Identify the preparation type.
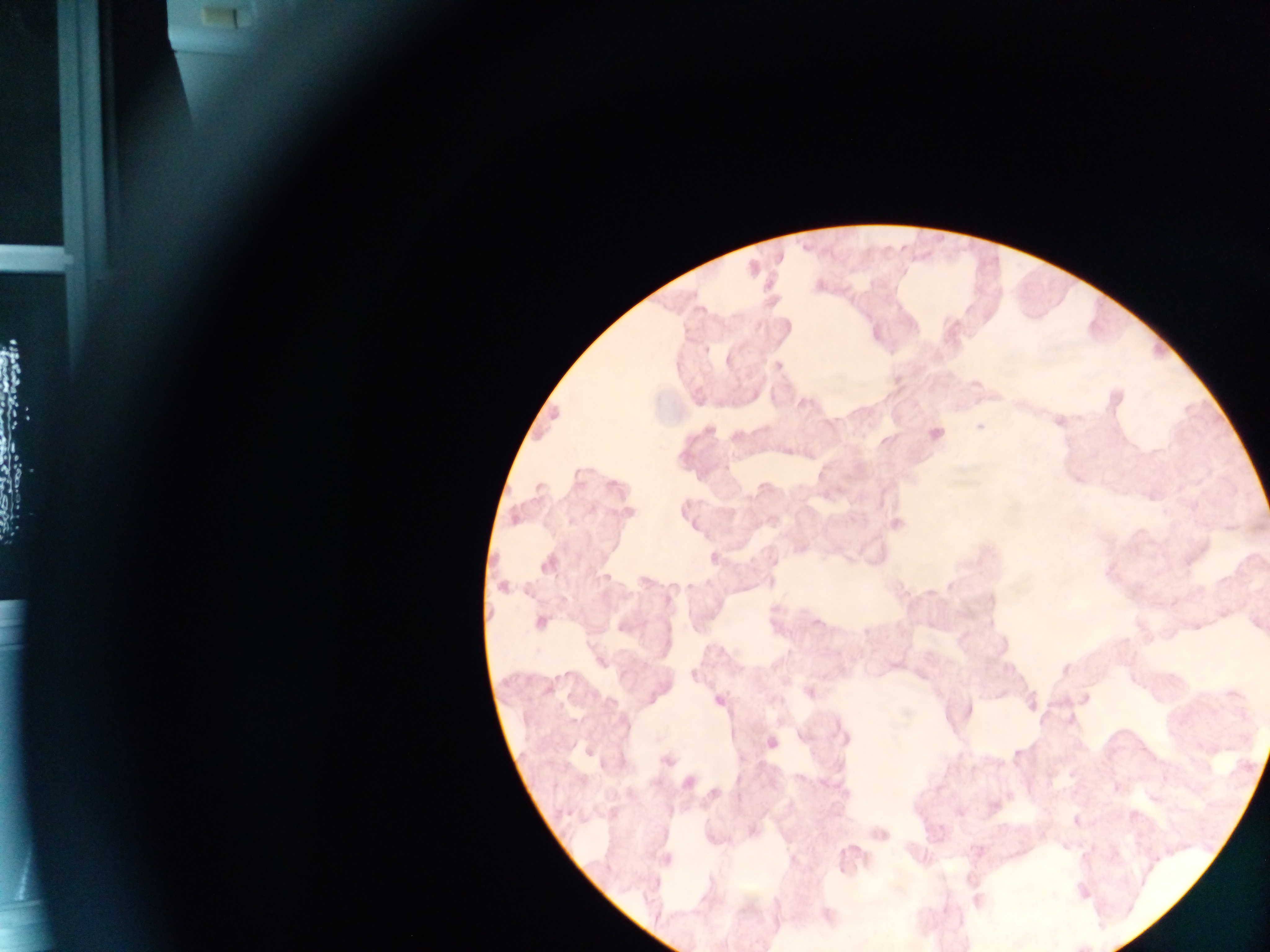

Thick blood film.

Approximate centers as {x, y} in pixels.
Summary:
  - Malaria parasite locations: {225, 16}, {968, 309}, {706, 349}, {778, 365}, {980, 427}, {710, 430}, {935, 434}, {630, 512}, {896, 524}, {547, 564}, {501, 586}, {540, 623}, {692, 675}, {719, 701}, {772, 742}, {667, 760}, {688, 782}
  - Country: Ghana
  - Capture: mobile-phone photograph through a microscope
  - Image size: 1270×952 pixels
  - Field of view: single